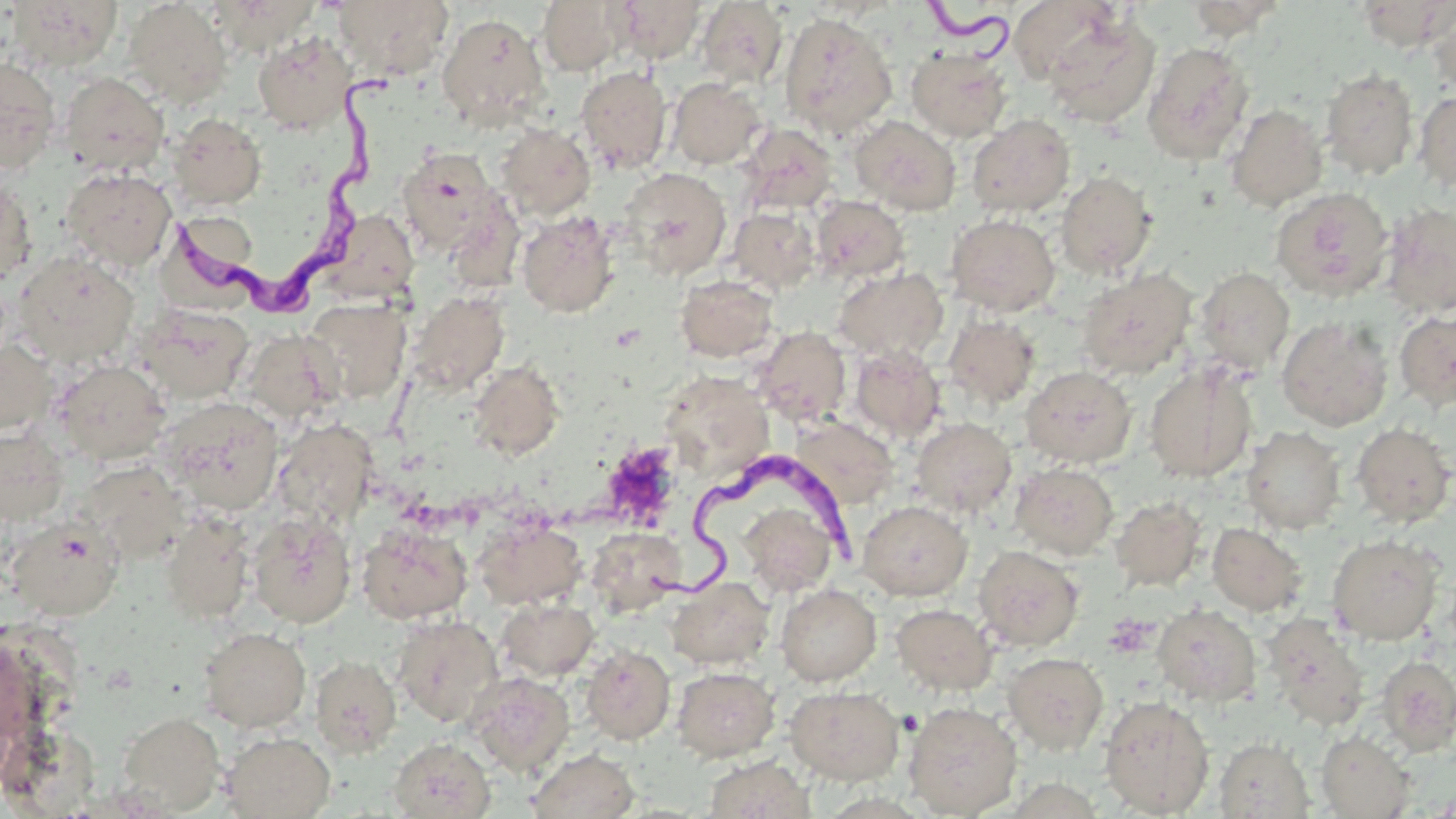
Approximate bounding boxes as (x1, y1, x2, y2) in pixels. Trypanosoma brucei locations: (913, 0, 1014, 70), (173, 74, 416, 326), (638, 451, 865, 615). Platelet locations: (602, 443, 681, 526). Uninfected red blood cell locations: (3, 0, 123, 72), (211, 0, 319, 55), (333, 0, 454, 81), (536, 0, 630, 76), (615, 0, 707, 63), (1007, 0, 1123, 85), (1183, 0, 1288, 40), (123, 1, 233, 108), (696, 1, 788, 89), (1355, 1, 1454, 51), (1427, 1, 1456, 95), (1040, 10, 1160, 127), (437, 13, 549, 129), (780, 13, 897, 140), (253, 31, 355, 134), (1142, 42, 1255, 164), (906, 46, 1013, 142), (0, 58, 61, 174), (576, 65, 673, 175), (1321, 68, 1418, 180), (59, 71, 169, 176), (667, 77, 767, 169), (1414, 89, 1456, 193), (1226, 104, 1328, 211), (167, 113, 266, 210), (967, 114, 1075, 217), (849, 115, 961, 215), (495, 122, 596, 220), (738, 124, 838, 215), (396, 149, 499, 254), (61, 167, 177, 271), (619, 167, 732, 280), (1056, 170, 1157, 278), (0, 178, 37, 287), (1271, 187, 1394, 301), (810, 195, 909, 282), (443, 196, 525, 295), (1382, 202, 1456, 319), (728, 206, 821, 292), (323, 208, 420, 304), (517, 211, 620, 318), (946, 214, 1061, 317), (13, 251, 140, 368), (833, 266, 949, 363), (1194, 267, 1295, 375), (1076, 268, 1197, 379), (675, 274, 779, 362), (407, 291, 509, 395), (303, 298, 411, 404), (133, 304, 254, 404), (1394, 309, 1456, 411), (943, 314, 1041, 409), (1276, 317, 1392, 431), (753, 326, 852, 426), (240, 328, 343, 423), (0, 339, 57, 435), (849, 345, 946, 442), (468, 359, 564, 461), (53, 360, 171, 464), (1144, 362, 1257, 482), (1021, 365, 1136, 468), (658, 372, 773, 478), (158, 396, 285, 514), (789, 416, 898, 509), (911, 417, 1016, 517), (271, 419, 378, 530), (1352, 422, 1455, 527), (1346, 423, 1450, 650), (1241, 426, 1346, 533), (1, 428, 68, 525), (77, 460, 190, 562), (1010, 462, 1118, 559), (1111, 496, 1206, 591), (736, 497, 841, 598), (858, 500, 972, 600), (159, 509, 255, 624), (248, 511, 356, 628), (4, 515, 125, 620), (474, 517, 587, 609), (357, 522, 472, 623), (1207, 523, 1308, 615), (586, 527, 686, 616), (1326, 534, 1444, 645), (974, 545, 1084, 651), (666, 576, 775, 669), (776, 583, 881, 685), (495, 598, 599, 681), (891, 603, 998, 695), (1152, 604, 1261, 707), (392, 614, 504, 726), (1262, 614, 1370, 730), (199, 627, 311, 732), (581, 644, 675, 743), (1003, 652, 1109, 755), (310, 654, 401, 757), (1376, 654, 1456, 754), (672, 666, 780, 761), (466, 672, 576, 776), (785, 685, 905, 784), (1099, 695, 1215, 817), (903, 700, 1022, 817), (117, 711, 225, 815), (1316, 731, 1415, 819), (221, 732, 336, 818), (388, 737, 495, 819), (1214, 737, 1314, 818), (527, 748, 640, 819), (704, 755, 815, 819). Slide-level diagnosis: Trypanosoma brucei. Image is 1456×819 pixels. Thin blood film. Single field of view. Optical microscopy. Captured at 1000x magnification. May-Grünwald-Giemsa stain.